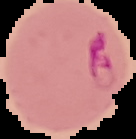
Summary:
  - Image type: cell region segmented out of the field of view; surrounding area masked to black
  - Preparation: thin blood smear
  - Image size: 136×139 pixels
  - Malaria status: parasitized